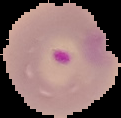
image type = cell region segmented out of the field of view; surrounding area masked to black
preparation = thin blood smear
result = Plasmodium parasites identified
image size = 121×118 pixels